Locate Plasmodium parasites and leukocytes.
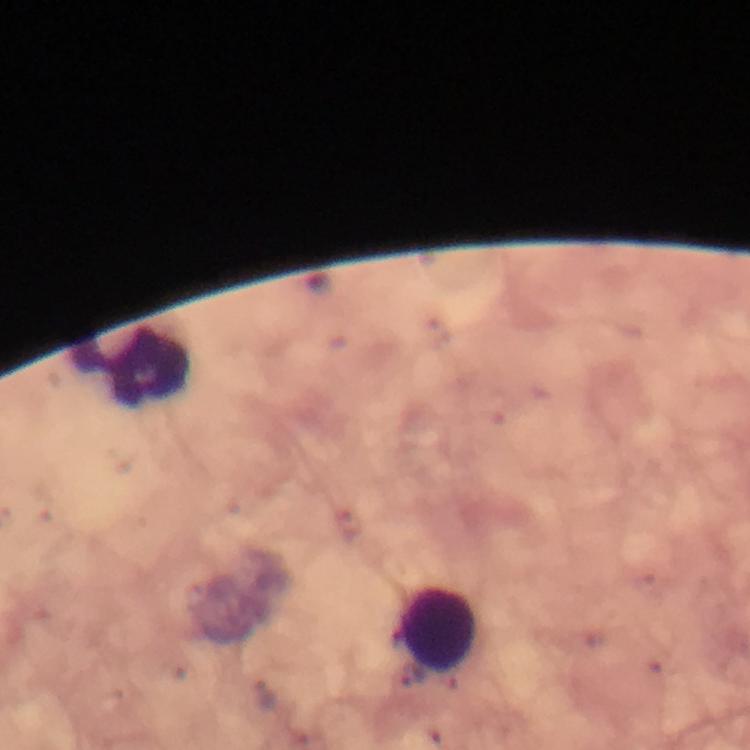

No Plasmodium parasites detected.
Approximate centers as [x, y] in pixels.
Leukocytes: [131, 368], [434, 629].

immersion oil = used
stain = Giemsa
context = from a diagnostic examination for malaria
image size = 750×750 pixels
capture = smartphone camera through the microscope
preparation = thick blood smear
magnification = 100x
cropped from = a single field of view